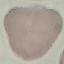

Summary:
  - Malaria status: uninfected
  - Stain: Giemsa
  - Image type: cell patch, automatically extracted from a larger field of view and resized to 64 × 64 pixels
  - Capture: smartphone camera at the microscope eyepiece
  - Preparation: thin blood smear